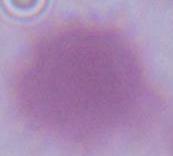
A red blood cell is seen. 1000x magnification. Photomicrograph.